Locate every Plasmodium parasite.
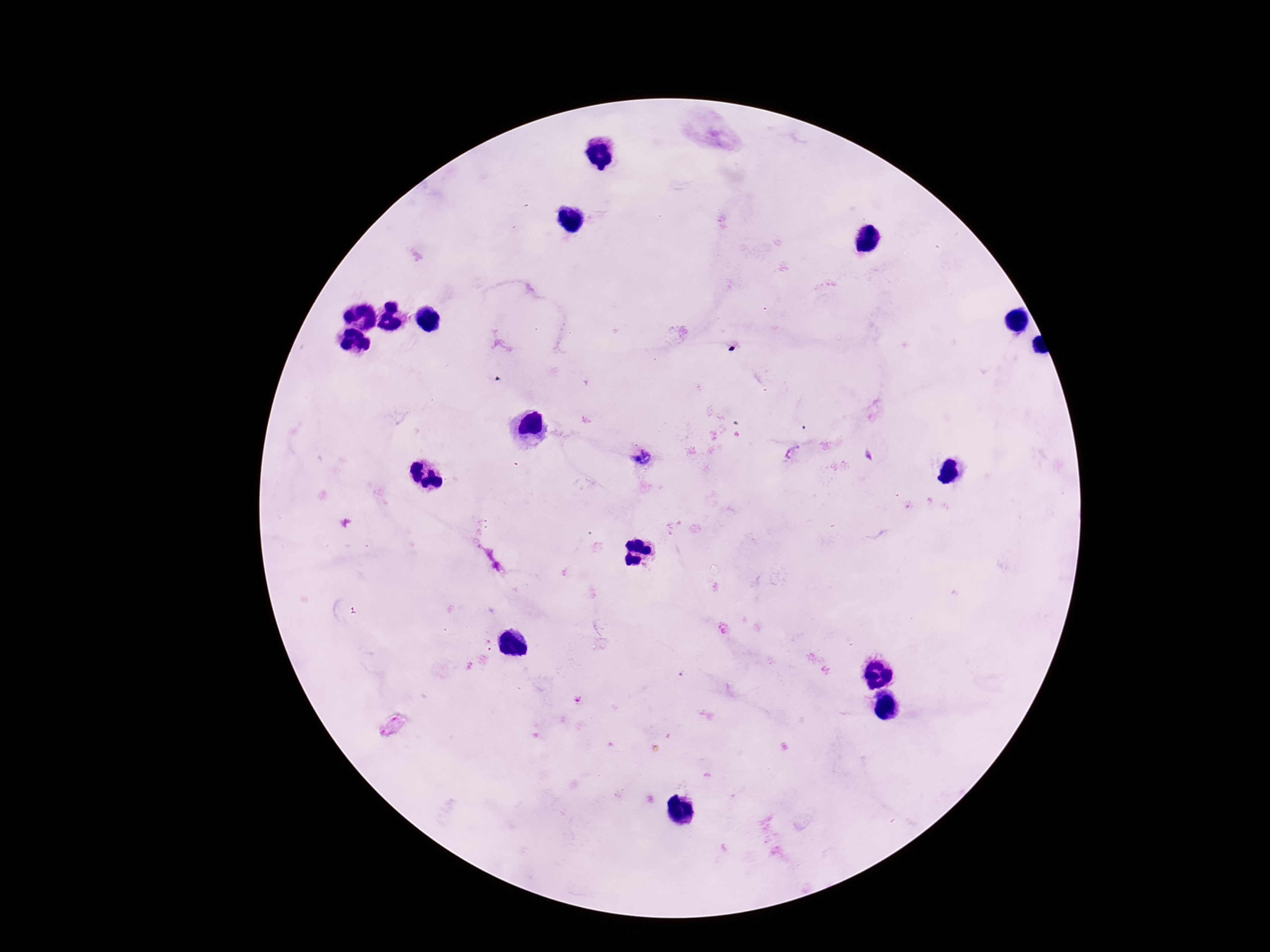

Approximate centers as (x, y) in pixels.
Plasmodium parasites: (793, 453), (641, 460), (577, 701), (392, 725).

Summary:
  - Magnification: 100x
  - Capture: smartphone camera through the microscope eyepiece
  - Preparation: thick blood smear
  - Field of view: single
  - Image size: 1270×952 pixels
  - Patient malaria status: positive
  - Stain: Giemsa